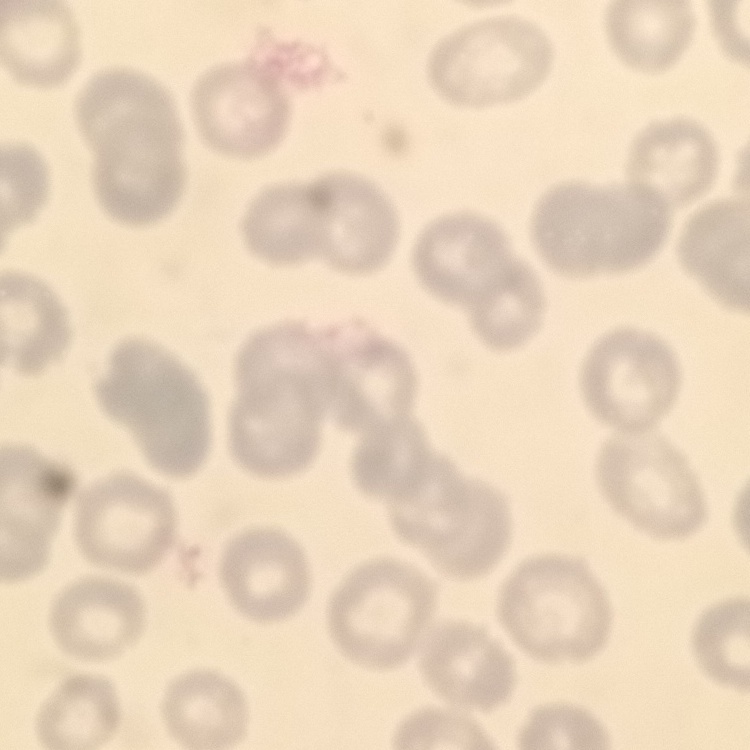 The red blood cells show no rouleaux formation. Thin blood film. Field's or Giemsa stain. Square crop of a larger photomicrograph.